Classify this cell by malaria status.
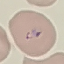
Parasitized.

preparation = thin blood smear
image type = automatically extracted cell patch, resized to 64 × 64 pixels
stain = Giemsa
capture = smartphone through the microscope eyepiece